Classify this cell by malaria status.
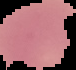
Uninfected.

image size = 76×70 pixels
image type = segmented cell region on a black background
preparation = thin blood smear